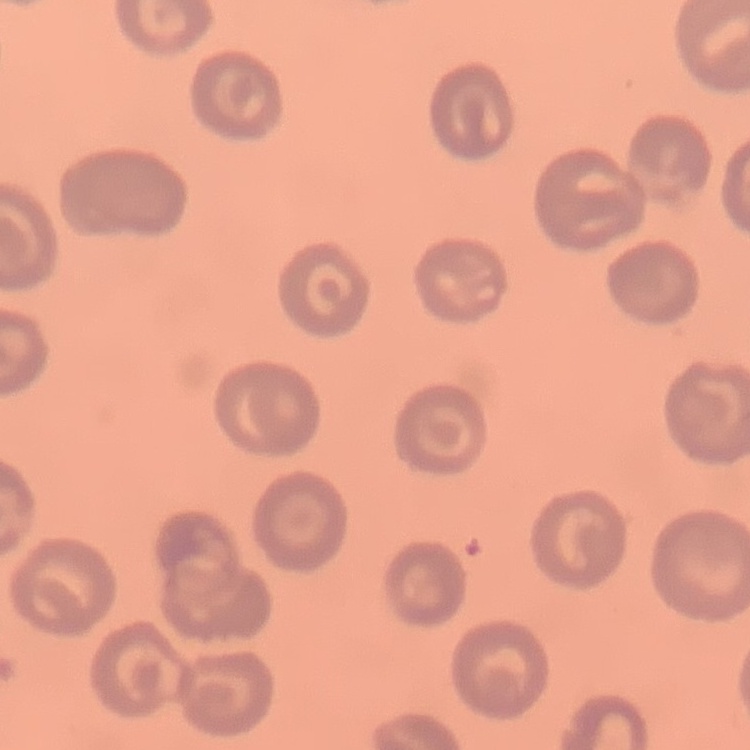

Summary:
  - Red blood cell morphology: no rouleaux formation
  - Image type: one tile cut from a larger photomicrograph
  - Preparation: thin blood film
  - Stain: Field's or Giemsa